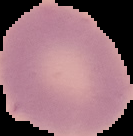
preparation = thin blood smear
image type = cell region segmented out of the field of view; surrounding area masked to black
result = negative for malaria parasites
image size = 133×136 pixels